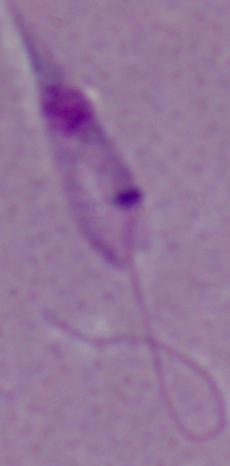 1000x magnification. Photomicrograph. A Leishmania parasite is seen.